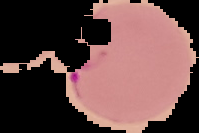
Summary:
  - Malaria status: parasitized
  - Image size: 199×133 pixels
  - Preparation: thin blood smear
  - Image type: segmented cell region on a black background